Evaluate for parasitized red blood cells.
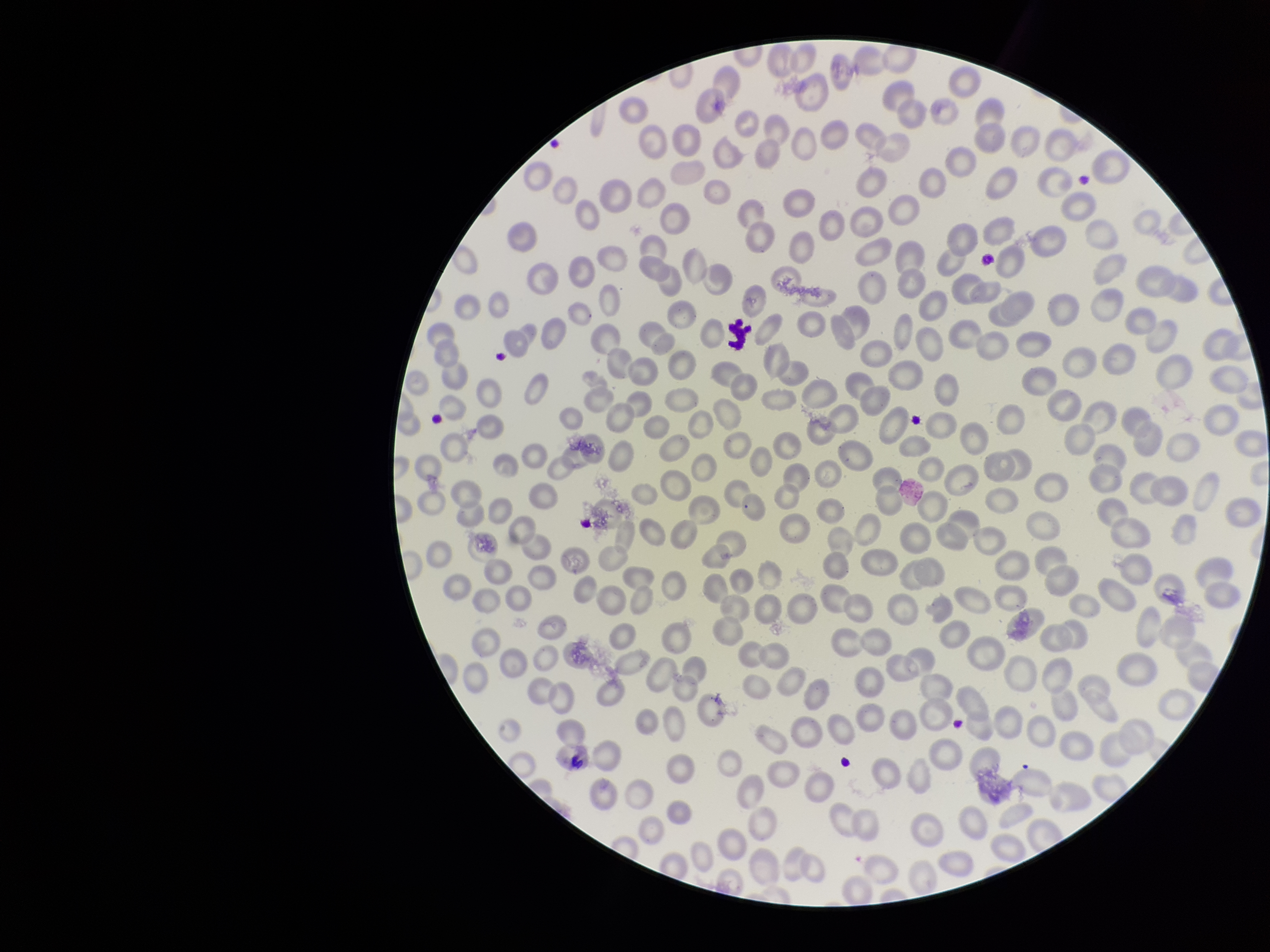

None seen.

image size = 1270×952 pixels
patient malaria status = negative
capture = smartphone photograph through the microscope eyepiece
red blood cell count = 298
parasitized red blood cell count = 0
stain = Giemsa
field of view = one from this slide
preparation = thin smear